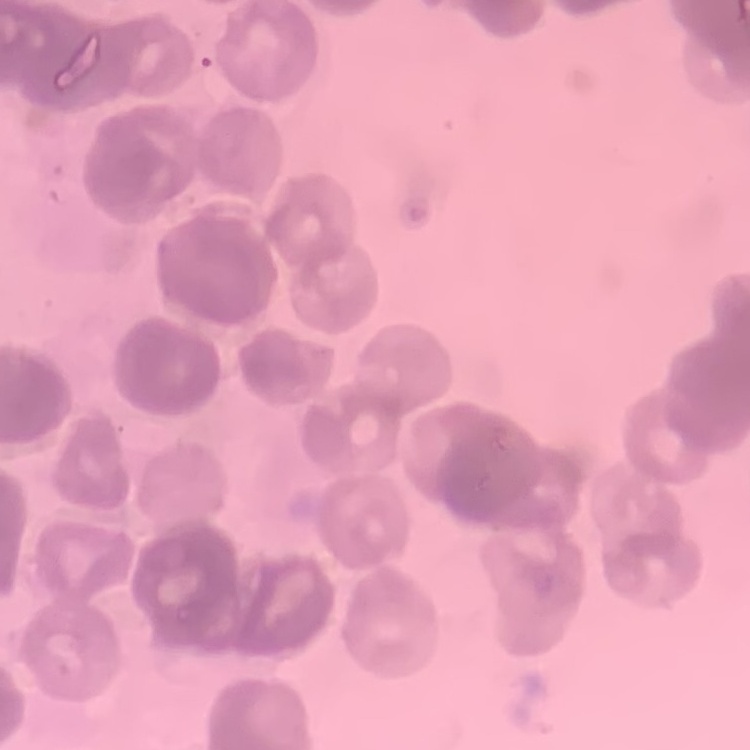
The erythrocytes show rouleaux formation. Thin peripheral smear. Stained with either Field's or Giemsa. One tile cut from a larger photomicrograph.